Give the extent of all uninfected red blood cells.
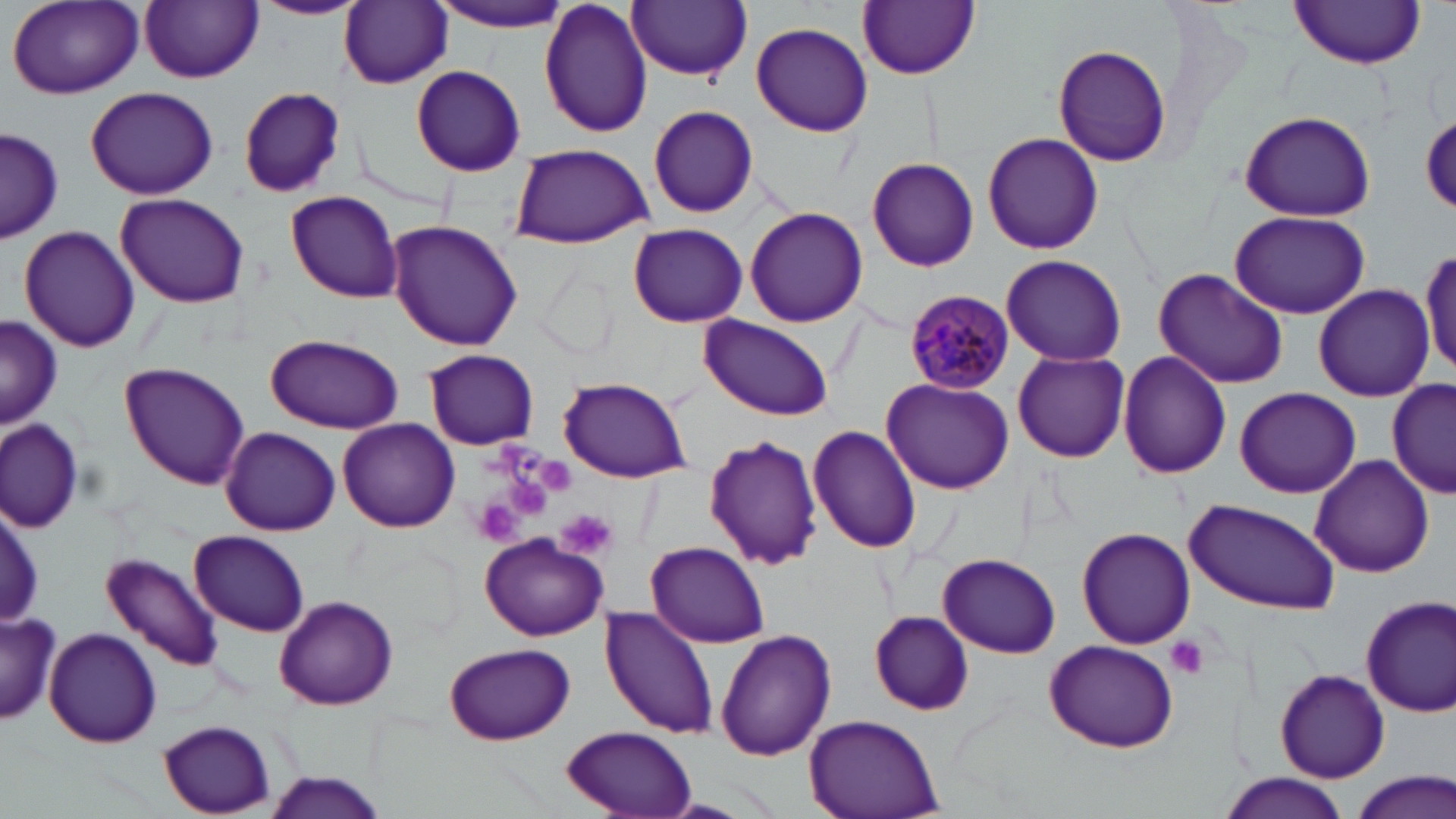

Approximate bounding boxes as (x1, y1, x2, y2) in pixels.
Uninfected red blood cells: (424, 0, 579, 32), (538, 0, 652, 139), (8, 1, 145, 100), (253, 1, 364, 20), (339, 1, 453, 88), (627, 1, 754, 81), (858, 1, 980, 80), (1287, 1, 1428, 69), (141, 2, 262, 83), (750, 22, 874, 137), (1051, 41, 1174, 167), (411, 64, 526, 176), (240, 86, 346, 198), (86, 87, 217, 201), (647, 104, 760, 218), (1236, 109, 1379, 224), (1421, 112, 1456, 213), (1, 126, 64, 242), (983, 132, 1103, 254), (505, 141, 657, 249), (866, 156, 980, 272), (285, 190, 404, 304), (116, 194, 251, 310), (744, 206, 868, 327), (1228, 210, 1369, 319), (386, 220, 524, 353), (628, 222, 748, 328), (19, 226, 141, 355), (1420, 248, 1456, 378), (998, 254, 1129, 368), (1153, 267, 1289, 389), (1313, 283, 1434, 400), (698, 313, 837, 422), (0, 316, 61, 428), (265, 333, 402, 435), (424, 349, 539, 450), (1013, 351, 1131, 464), (1117, 353, 1231, 480), (120, 362, 250, 490), (558, 376, 690, 484), (881, 377, 1015, 495), (1387, 380, 1455, 502), (1234, 387, 1361, 499), (0, 416, 87, 532), (337, 418, 459, 532), (808, 425, 921, 554), (221, 427, 342, 534), (703, 433, 826, 573), (1309, 453, 1434, 577), (1182, 498, 1341, 613), (2, 500, 44, 632), (1075, 526, 1196, 648), (190, 530, 308, 635), (481, 534, 608, 640), (645, 541, 769, 647), (937, 552, 1061, 658), (102, 553, 224, 672), (1358, 594, 1456, 718), (274, 595, 399, 709), (600, 608, 720, 740), (0, 611, 61, 728), (869, 611, 974, 714), (43, 627, 163, 748), (714, 629, 837, 762), (1044, 640, 1180, 752), (444, 642, 575, 745), (1275, 668, 1390, 783), (802, 715, 946, 818), (158, 721, 279, 816), (559, 724, 698, 818), (260, 771, 390, 818), (1347, 771, 1456, 819), (1219, 775, 1351, 818).

{
  "slide_level_diagnosis": "Plasmodium malariae",
  "stain": "May-Grünwald-Giemsa",
  "preparation": "thin blood film",
  "plasmodium_malariae_infected_red_blood_cell_locations": "approximate bounding boxes as (x1, y1, x2, y2) in pixels: (905, 290, 1015, 395)",
  "modality": "light microscopy",
  "platelet_locations": "approximate bounding boxes as (x1, y1, x2, y2) in pixels: (535, 458, 576, 494), (505, 475, 550, 515), (472, 500, 523, 546), (555, 508, 619, 559), (1165, 634, 1210, 681)",
  "field_of_view": "single",
  "image_size": "1456×819 pixels",
  "magnification": "1000x"
}